Report the malaria status of this cell.
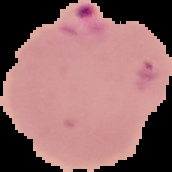
It is parasitized.

Image is 172×172 pixels. From a thin blood smear. Cell region segmented out of the field of view; the surrounding area is masked to black.